Report the malaria status of this cell.
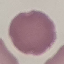

It is uninfected.

Photographed with a smartphone camera at the microscope eyepiece. Automatically extracted cell patch, resized to 64 × 64 pixels. Giemsa stain. Thin blood film.